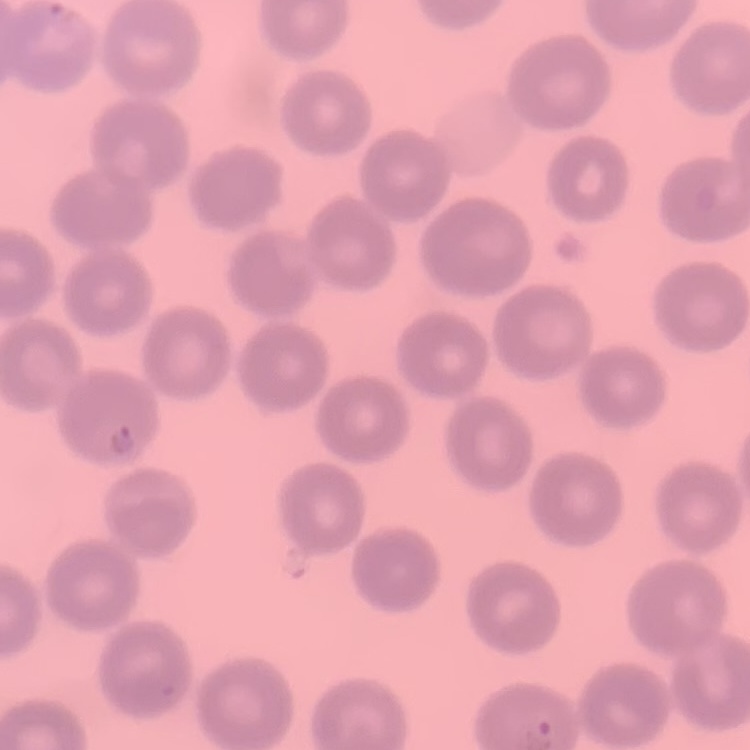 The erythrocytes show no rouleaux formation. Square crop of a larger photomicrograph. Stained with either Field's or Giemsa. Thin peripheral smear.